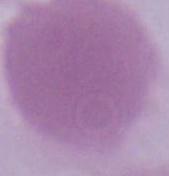
identification = erythrocyte
modality = micrograph
magnification = 1000x